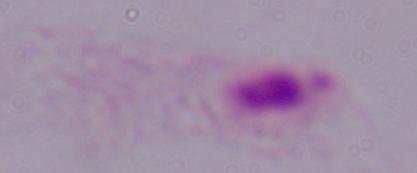
Summary:
  - Magnification: 1000x
  - Identification: trichomonad
  - Modality: micrograph